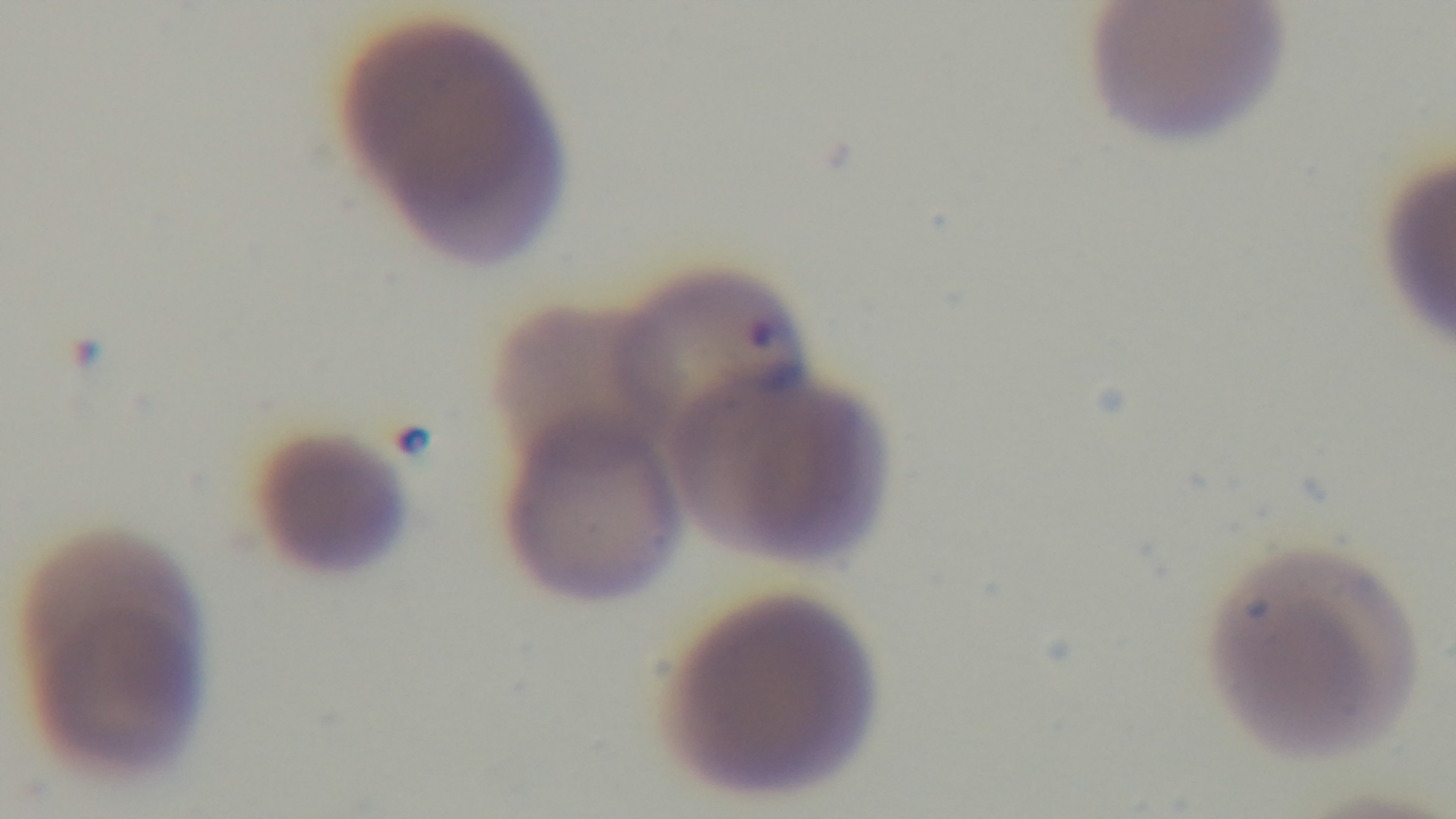
preparation = thin blood film
malaria status = positive
stain = Giemsa
field of view = one from the slide
objective = 100x oil immersion
capture = mounted 4K digital camera
modality = light microscopy